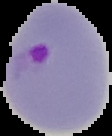

Segmented cell region on a black background. Result: malaria parasites identified. Image is 112×136 pixels. From a thin blood film.